Report the malaria status of this cell.
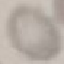

Uninfected.

preparation = thin blood smear
image type = automatically extracted cell patch, resized to 64 × 64 pixels
stain = Giemsa
capture = smartphone camera at the microscope eyepiece